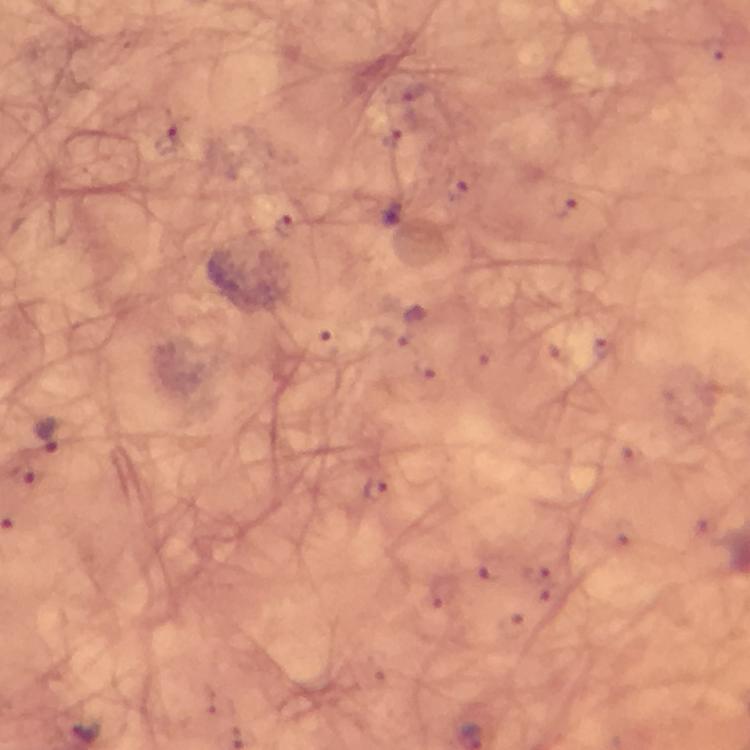
Approximate centers as [x, y] in pixels. Malaria parasite locations: [170, 141], [284, 224], [324, 347], [45, 434], [376, 488], [87, 729]. Cropped region of a single field of view. Thick blood smear. Image is 750×750 pixels. Photographed with a smartphone mounted on the microscope. Giemsa-stained preparation. Immersion oil applied. At 100x magnification. From a diagnostic examination for malaria.